Name the parasite shown.
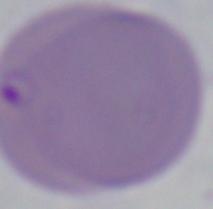
This is Babesia.

Summary:
  - Magnification: 1000x
  - Modality: micrograph